Report the malaria status of this cell.
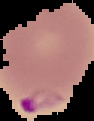
Parasitized.

Image is 94×121 pixels. From a thin blood smear. The area outside the segmented cell region is set to black.